Assess this cell for malaria.
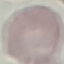

It is uninfected.

Cell patch, automatically extracted from a larger field of view and resized to 64 × 64 pixels. Acquired by smartphone through the microscope eyepiece. Giemsa stain. Thin blood smear.